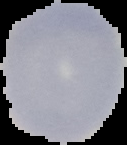
preparation: thin blood smear
image_size: 127×145 pixels
image_type: segmented cell region with the area outside set to black
malaria_status: uninfected